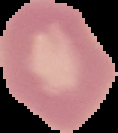
Summary:
  - Preparation: thin blood film
  - Image size: 118×133 pixels
  - Malaria status: uninfected
  - Image type: segmented cell region with the area outside set to black